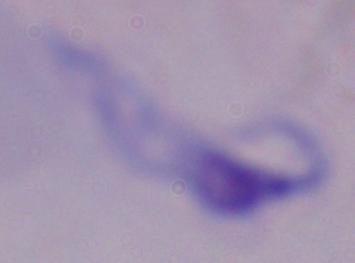

A trypanosome is shown. Micrograph. Captured at 1000x magnification.